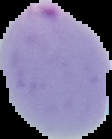
Summary:
  - Image type: segmented cell region on a black background
  - Preparation: thin blood film
  - Image size: 112×139 pixels
  - Result: Plasmodium parasites identified